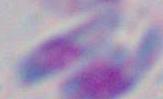

{
  "modality": "micrograph",
  "identification": "Toxoplasma gondii",
  "magnification": "1000x"
}